State the preparation type.
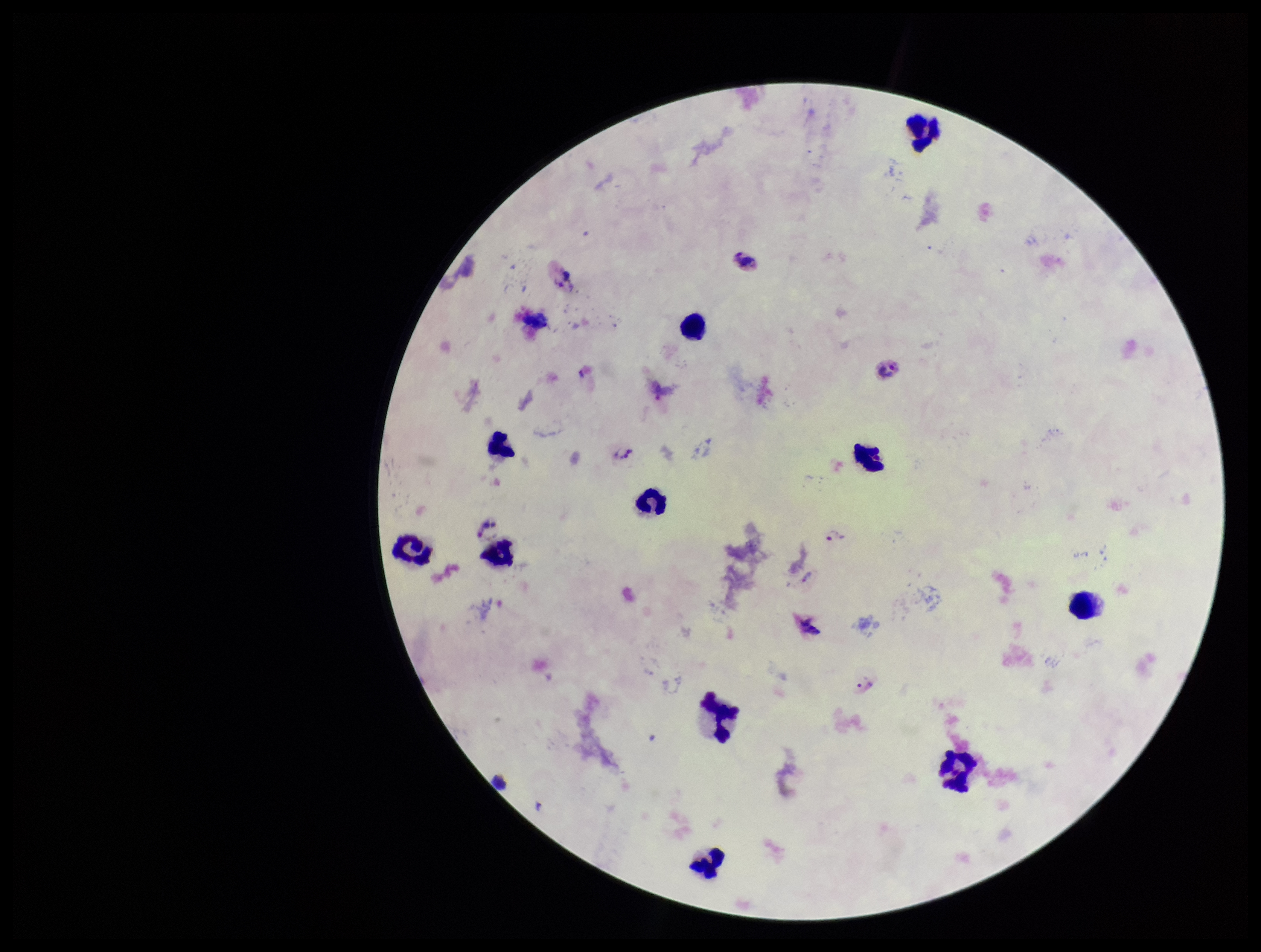
Thick.

field of view = single
stain = Giemsa
parasite count = 3
patient malaria status = positive
capture = smartphone photograph through the microscope eyepiece
leukocyte count = 11
Plasmodium parasites = detected
image size = 1261×952 pixels
species reported for this patient = Plasmodium vivax